Report the malaria status of this cell.
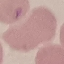
It is uninfected.

Summary:
  - Capture: smartphone camera at the microscope eyepiece
  - Preparation: thin blood smear
  - Stain: Giemsa
  - Image type: automatically extracted cell patch, resized to 64 × 64 pixels